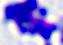
{
  "magnification": "400x",
  "identification": "leukocyte",
  "modality": "micrograph"
}